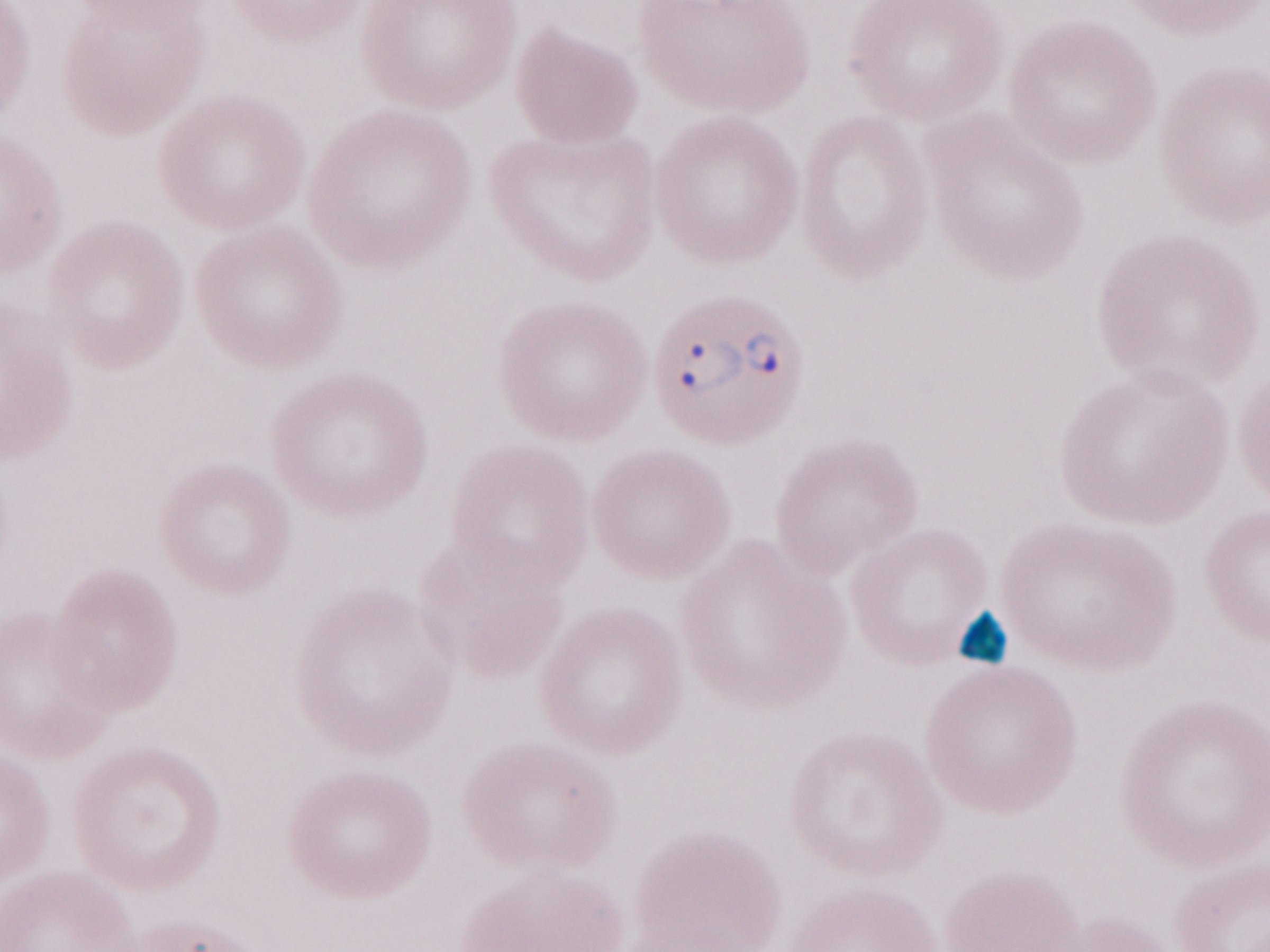

Image is 1270×952 pixels. Olympus BX43 microscope, Olympus DP73 camera. Single field of view. Magnification: 1,000x. May-Grünwald-Giemsa (MGG) stain. Malaria diagnosis (patient-level): positive. Thin blood film.